Assess the morphology of the erythrocytes.
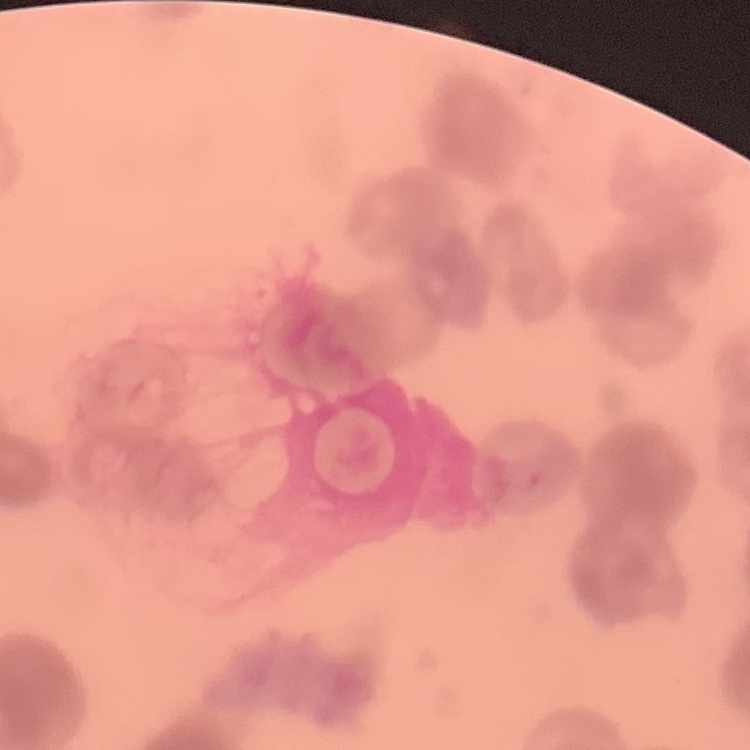

They show rouleaux formation.

stain = Field's or Giemsa
preparation = thin blood film
image type = one tile cut from a larger photomicrograph